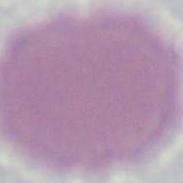

identification = red blood cell
magnification = 1000x
modality = photomicrograph